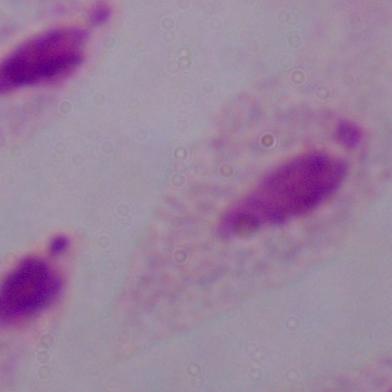
Summary:
  - Modality: micrograph
  - Identification: trichomonad
  - Magnification: 1000x